Assess the morphology of the erythrocytes.
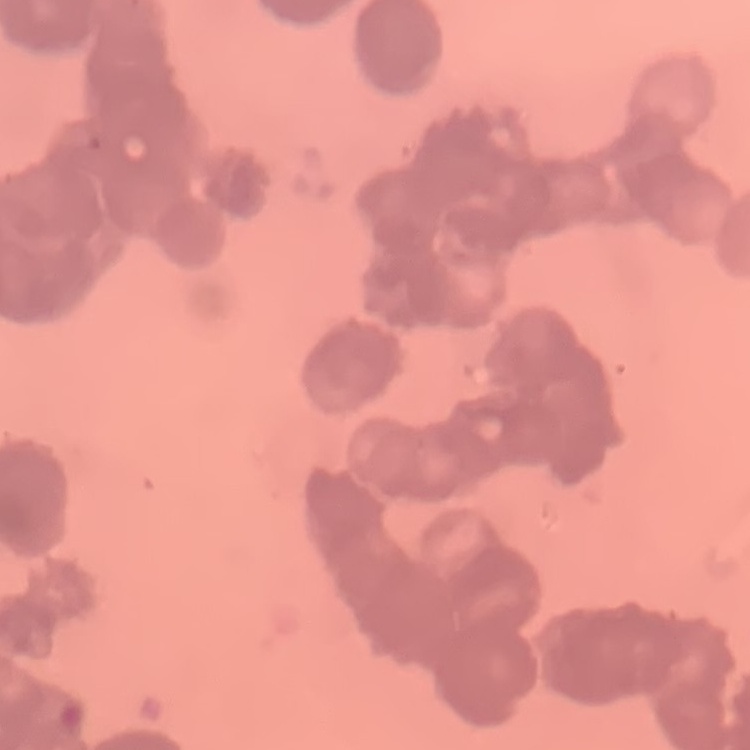
Rouleaux formation.

Summary:
  - Image type: square crop of a larger photomicrograph
  - Preparation: thin blood film
  - Stain: Field's or Giemsa